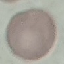
Summary:
  - Malaria status: uninfected
  - Capture: smartphone camera at the microscope eyepiece
  - Stain: Giemsa
  - Preparation: thin blood smear
  - Image type: automatically extracted cell patch, resized to 64 × 64 pixels